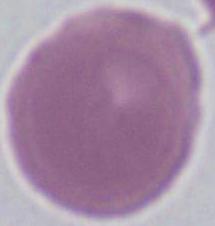
identification = erythrocyte
magnification = 1000x
modality = photomicrograph